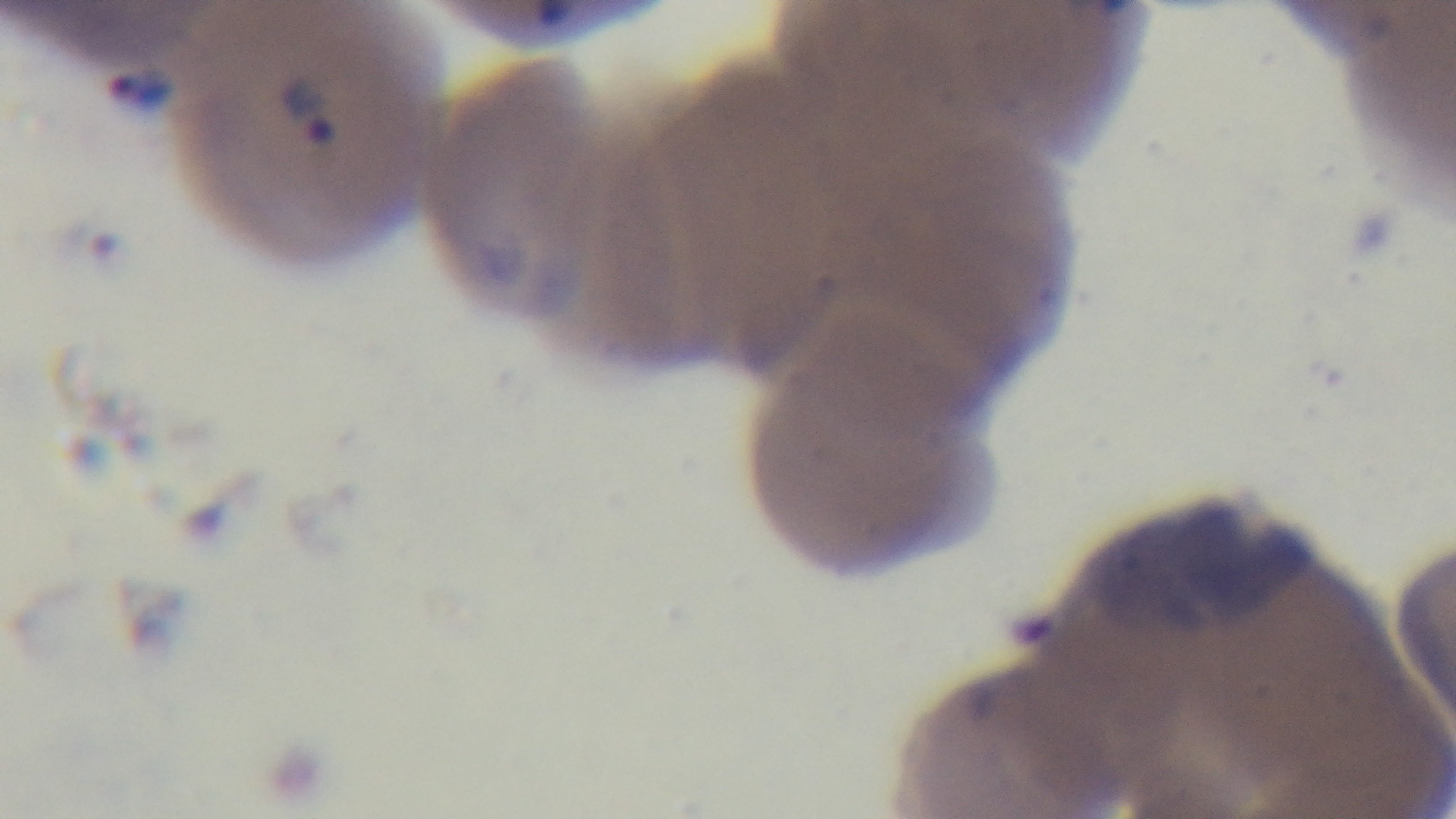
field of view = one from the slide
capture = mounted 4K digital camera
modality = light microscopy
stain = Giemsa
preparation = thin smear
objective = 100x oil immersion
malaria status = infected